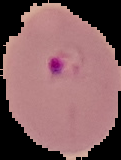
{
  "image_type": "segmented cell region with the area outside set to black",
  "result": "Plasmodium parasites identified",
  "preparation": "thin blood film",
  "image_size": "121×160 pixels"
}